Classify this cell by malaria status.
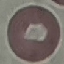
It is uninfected.

Giemsa stain. Thin blood film. Cell patch, automatically extracted from a larger field of view and resized to 64 × 64 pixels. Acquired by smartphone through the microscope eyepiece.